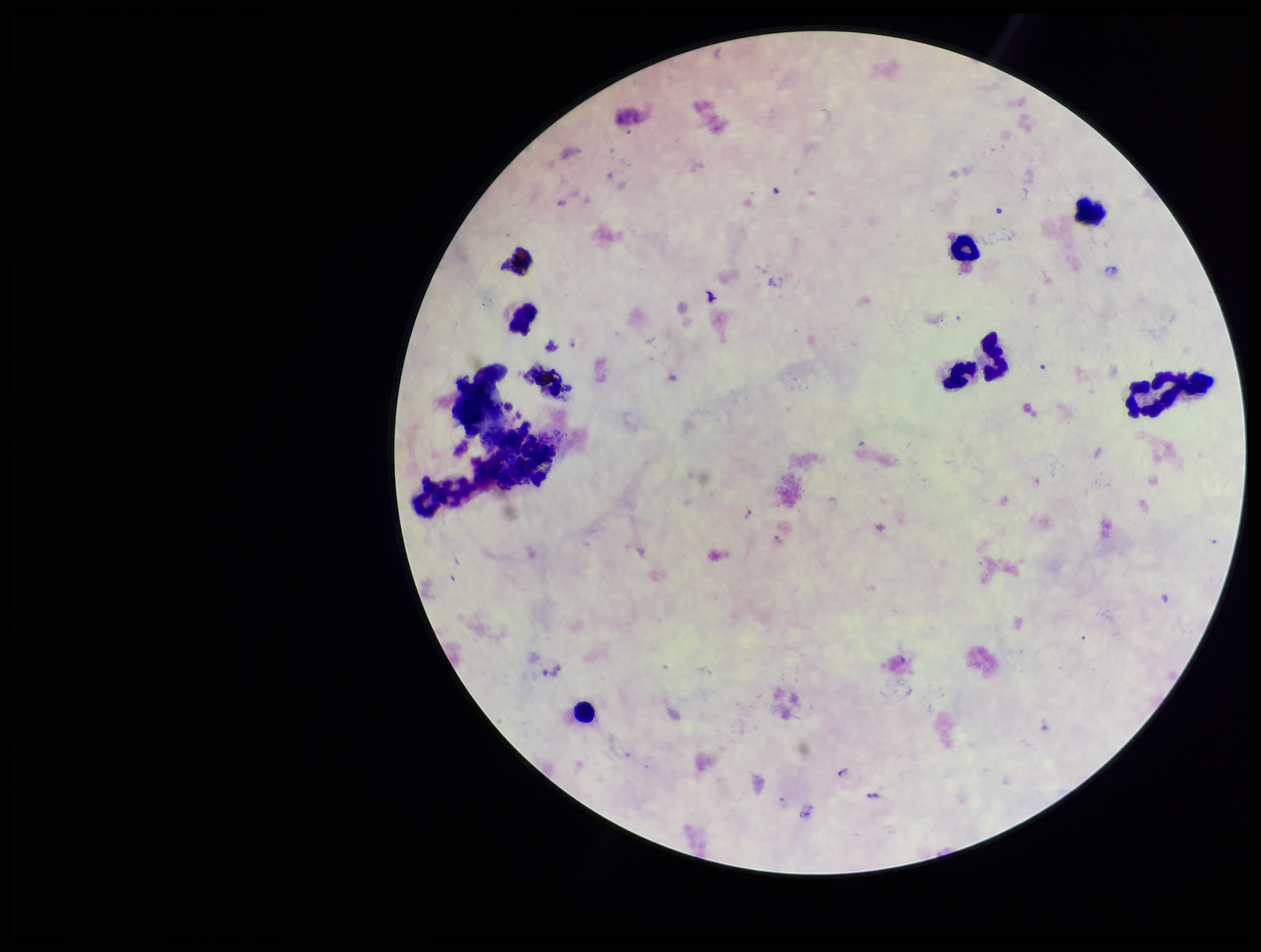
One field from this slide. Image is 1261×952 pixels. Stained with Giemsa. Leukocyte count: 7. Preparation: thick blood smear. Species reported for this patient: Plasmodium falciparum. Patient malaria status: infected. Plasmodium parasites: identified. Parasite count: 4. Smartphone photograph taken through the eyepiece of a microscope.